Mark where platelets are.
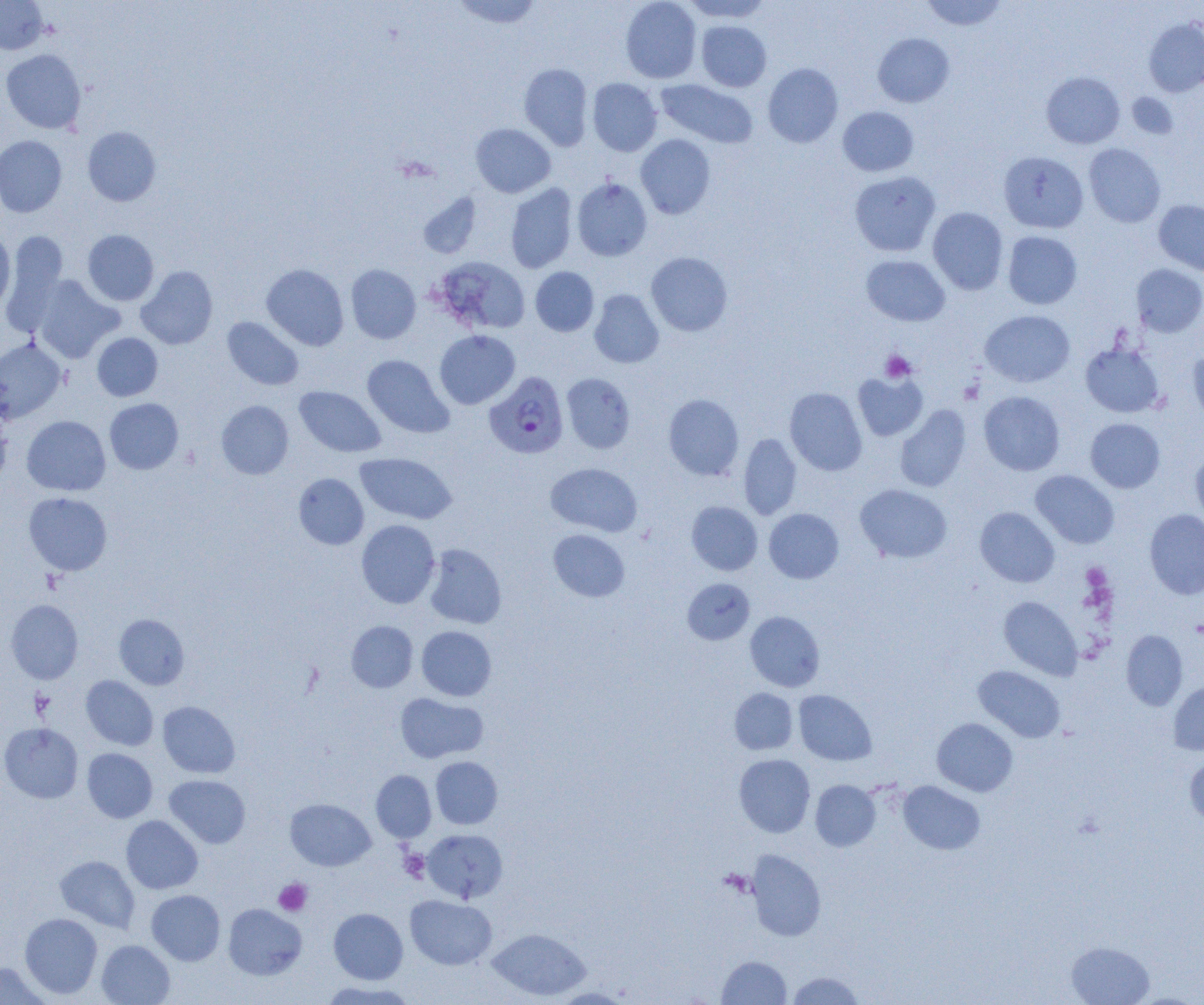
Approximate bounding boxes as [x1, y1, x2, y2] in pixels.
Platelets: [1127, 92, 1179, 138], [880, 350, 916, 382], [960, 380, 984, 404], [399, 850, 430, 882], [273, 878, 312, 916].

Plasmodium falciparum-infected red blood cell locations: [484, 371, 569, 458]. Uninfected red blood cell locations: [0, 0, 49, 54], [452, 0, 543, 30], [620, 0, 702, 83], [681, 0, 773, 23], [920, 0, 1008, 31], [1143, 17, 1204, 97], [696, 20, 771, 91], [873, 33, 955, 107], [1, 49, 86, 134], [518, 63, 593, 151], [763, 63, 843, 147], [1041, 71, 1124, 149], [588, 78, 662, 156], [656, 79, 758, 148], [838, 106, 919, 176], [471, 123, 556, 198], [83, 126, 161, 206], [636, 134, 716, 219], [0, 135, 67, 217], [1084, 143, 1166, 227], [998, 151, 1088, 233], [850, 171, 940, 257], [572, 178, 652, 261], [505, 183, 578, 273], [418, 193, 480, 258], [1154, 200, 1204, 275], [927, 207, 1008, 295], [82, 229, 159, 305], [1003, 231, 1082, 309], [3, 232, 68, 335], [0, 233, 15, 312], [646, 252, 732, 336], [861, 255, 950, 326], [434, 257, 530, 335], [261, 264, 349, 351], [346, 264, 421, 344], [1132, 264, 1204, 337], [136, 266, 218, 349], [530, 267, 599, 336], [31, 275, 123, 363], [589, 289, 664, 368], [980, 310, 1075, 387], [222, 317, 303, 390], [434, 330, 520, 409], [92, 333, 163, 401], [0, 337, 66, 423], [1080, 342, 1165, 417], [1187, 348, 1204, 424], [362, 355, 453, 438], [852, 370, 928, 441], [561, 373, 636, 454], [294, 386, 386, 457], [785, 387, 867, 475], [979, 391, 1065, 475], [663, 393, 744, 480], [104, 398, 183, 474], [216, 400, 293, 479], [895, 405, 971, 492], [0, 409, 13, 485], [22, 415, 110, 496], [1085, 418, 1165, 493], [738, 433, 802, 520], [1190, 449, 1204, 530], [355, 452, 457, 524], [545, 463, 642, 537], [1030, 470, 1119, 549], [293, 473, 369, 549], [855, 484, 952, 563], [23, 492, 112, 575], [686, 501, 763, 575], [975, 507, 1059, 587], [764, 508, 844, 583], [1144, 510, 1204, 599], [356, 519, 440, 608], [548, 529, 630, 602], [424, 544, 506, 629], [682, 578, 755, 645], [998, 596, 1082, 680], [6, 600, 83, 683], [745, 611, 825, 691], [114, 614, 190, 689], [346, 621, 418, 692], [416, 626, 497, 701], [1121, 630, 1188, 710], [973, 665, 1065, 743], [81, 675, 158, 750], [1168, 679, 1204, 755], [730, 688, 798, 755], [794, 690, 877, 766], [395, 692, 488, 763], [157, 701, 240, 778], [932, 718, 1018, 796], [0, 723, 83, 803], [82, 748, 158, 823], [734, 754, 815, 837], [1184, 754, 1204, 828], [430, 756, 502, 829], [371, 770, 436, 842], [164, 774, 251, 848], [810, 779, 881, 851], [898, 781, 985, 854], [285, 798, 375, 871], [121, 815, 203, 894], [422, 829, 508, 902], [746, 850, 826, 941], [55, 855, 140, 932], [146, 890, 225, 965], [405, 895, 496, 969], [223, 904, 307, 980], [328, 908, 408, 984], [20, 913, 103, 999], [487, 927, 591, 1001], [96, 940, 175, 1005], [1066, 941, 1155, 1005], [716, 956, 791, 1004], [0, 961, 49, 1004], [786, 971, 865, 1004], [318, 980, 415, 1005], [551, 987, 633, 1004]. Slide-level diagnosis: Plasmodium falciparum. Single field of view. Captured at 1000x magnification. Image is 1204×1005 pixels. Thin blood film. Light microscopy.